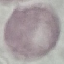
Summary:
  - Result: negative for malaria parasites
  - Capture: smartphone through the microscope eyepiece
  - Preparation: thin smear
  - Image type: cell patch, automatically extracted from a larger field of view and resized to 64 × 64 pixels
  - Stain: Giemsa